State which parasite is depicted.
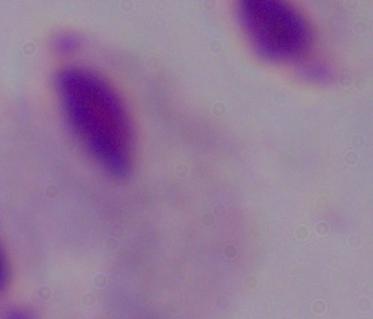

A trichomonad.

modality: micrograph
magnification: 1000x